Evaluate for malaria.
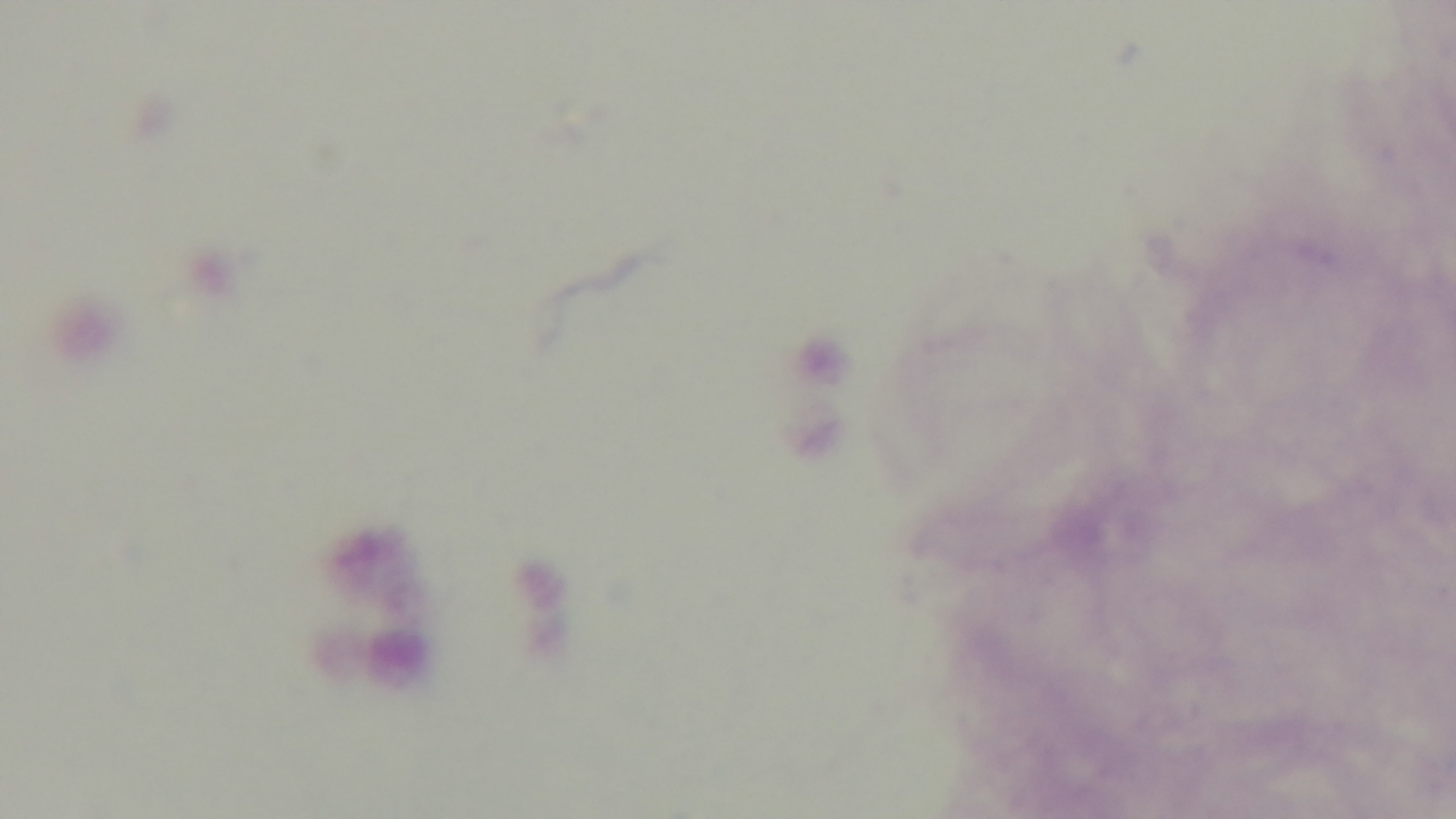

Negative.

Mounted 4K digital camera. Single field of view. Photomicrograph. Preparation: thick smear. Giemsa stain. Oil-immersion objective, 100x.